Give the extent of all uninfected red blood cells.
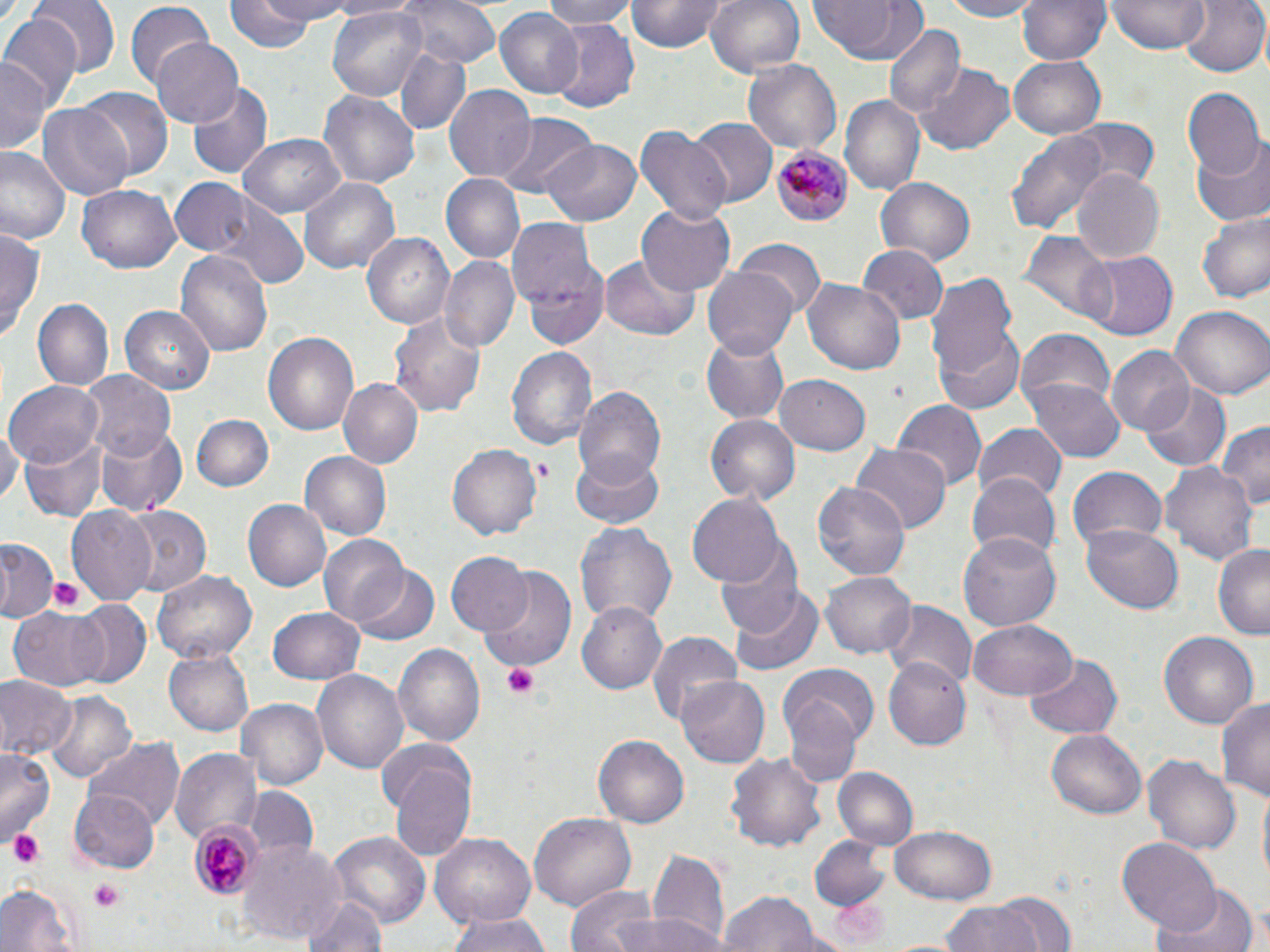
Approximate bounding boxes as (x1,y1)-(x2,y2) corner pairs in pixels.
Uninfected red blood cells: (33,0)-(118,78), (226,0)-(326,50), (243,0)-(354,27), (401,0)-(502,69), (539,0)-(637,28), (627,0)-(727,53), (704,0)-(806,78), (807,0)-(926,66), (938,0)-(1046,21), (1019,0)-(1111,66), (1109,0)-(1206,54), (1178,0)-(1268,78), (126,4)-(213,90), (325,5)-(428,102), (495,7)-(584,98), (0,13)-(82,108), (548,19)-(639,112), (885,27)-(965,119), (150,39)-(243,128), (394,49)-(470,136), (1010,55)-(1106,137), (2,56)-(47,155), (743,58)-(843,156), (917,66)-(1014,153), (187,83)-(272,180), (446,86)-(538,182), (1184,87)-(1264,179), (75,88)-(173,181), (320,91)-(419,189), (838,94)-(924,195), (38,104)-(134,203), (496,112)-(595,198), (688,118)-(776,206), (1069,118)-(1157,190), (634,125)-(730,224), (1007,127)-(1110,238), (238,134)-(346,217), (541,139)-(640,226), (1190,139)-(1270,226), (0,148)-(69,246), (1072,169)-(1165,263), (440,173)-(525,262), (298,175)-(402,275), (874,175)-(975,265), (167,179)-(257,257), (79,184)-(180,274), (213,202)-(306,290), (636,205)-(735,291), (1196,212)-(1270,303), (509,222)-(606,327), (0,229)-(44,340), (361,231)-(455,331), (1022,232)-(1115,323), (736,240)-(824,322), (859,245)-(949,327), (176,250)-(273,356), (1076,251)-(1180,341), (441,255)-(518,352), (600,256)-(700,341), (523,261)-(609,350), (704,264)-(799,360), (927,274)-(1021,382), (804,278)-(907,375), (31,299)-(114,390), (1170,303)-(1270,401), (120,304)-(215,393), (390,311)-(486,417), (933,324)-(1027,415), (262,329)-(359,437), (1015,329)-(1117,418), (702,332)-(790,424), (507,346)-(595,450), (1107,347)-(1193,437), (77,367)-(175,460), (775,375)-(871,455), (1028,377)-(1125,462), (339,378)-(424,467), (6,380)-(105,467), (1140,383)-(1230,470), (573,384)-(668,485), (891,399)-(988,489), (706,413)-(800,504), (190,415)-(274,493), (1216,421)-(1270,512), (95,423)-(188,518), (975,424)-(1067,503), (0,425)-(20,510), (20,436)-(107,521), (850,444)-(949,536), (448,446)-(541,540), (570,449)-(663,529), (298,450)-(391,541), (1164,462)-(1258,568), (1067,465)-(1167,556), (965,473)-(1060,562), (813,482)-(909,581), (687,492)-(785,587), (244,499)-(333,592), (66,507)-(156,602), (121,507)-(211,596), (575,519)-(678,629), (1083,526)-(1184,614), (959,531)-(1061,633), (318,535)-(409,627), (714,539)-(804,637), (0,540)-(55,622), (1212,543)-(1270,638), (445,552)-(531,636), (350,566)-(438,645), (152,569)-(257,664), (483,569)-(576,671), (821,571)-(916,659), (728,589)-(823,675), (578,600)-(668,695), (71,601)-(152,688), (882,604)-(975,688), (268,606)-(366,685), (8,609)-(109,691), (968,619)-(1075,701), (645,629)-(743,724), (1158,630)-(1259,728), (392,642)-(485,749), (165,649)-(253,737), (1024,654)-(1123,740), (882,658)-(972,751), (783,666)-(880,751), (312,669)-(408,774), (0,675)-(74,762), (676,678)-(770,767), (43,687)-(138,784), (782,695)-(863,787), (1216,696)-(1270,801), (235,698)-(327,791), (1046,729)-(1148,819), (592,735)-(690,827), (88,738)-(185,829), (379,740)-(479,858), (171,745)-(260,844), (0,746)-(55,845), (727,748)-(826,854), (1142,753)-(1240,855), (835,768)-(919,851), (1255,785)-(1270,891), (247,786)-(317,857), (71,789)-(161,873), (529,811)-(635,912), (890,826)-(996,904), (325,832)-(432,928), (810,834)-(891,911), (430,835)-(535,928), (1118,839)-(1221,933), (239,840)-(347,942), (648,847)-(731,952), (0,881)-(80,952), (1150,881)-(1262,952), (563,883)-(661,952), (715,891)-(828,952), (995,891)-(1075,952), (300,893)-(386,952), (941,901)-(1045,952), (446,912)-(552,952), (600,912)-(721,952).

Plasmodium malariae-infected red blood cell locations: (770,145)-(854,227), (188,816)-(265,898). Platelet locations: (534,458)-(551,479), (48,575)-(86,614), (501,661)-(542,698), (7,829)-(45,869), (90,879)-(126,909). Slide-level diagnosis: Plasmodium malariae. Thin blood film. Light microscopy. Captured at 1000x magnification. May-Grünwald-Giemsa stain. One field of a larger specimen. Image is 1270×952 pixels.